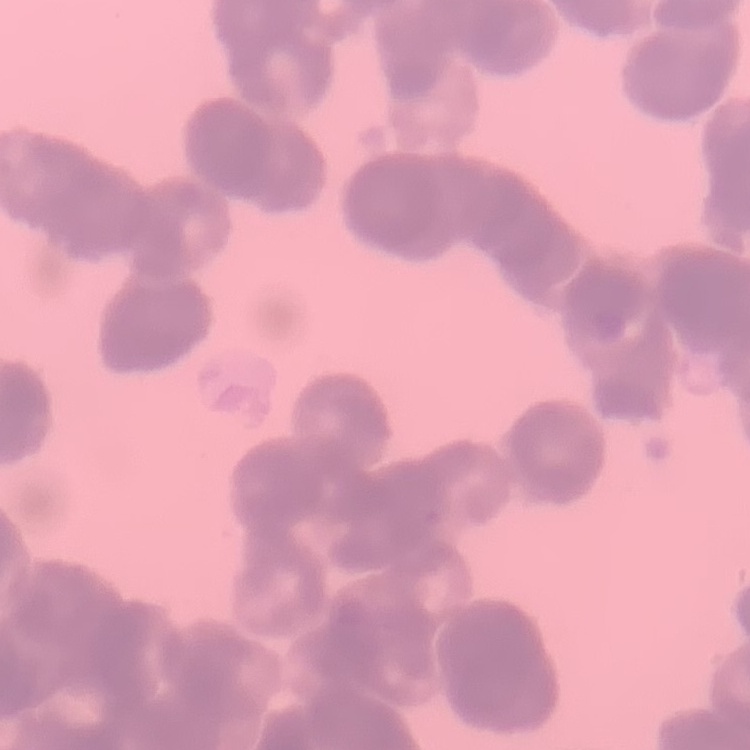

Summary:
  - Erythrocyte morphology: rouleaux formation
  - Preparation: thin blood film
  - Stain: Field's or Giemsa
  - Image type: square crop of a larger photomicrograph